Assess this cell for malaria.
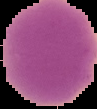

Uninfected.

image_type: cell region segmented out of the field of view; surrounding area masked to black
image_size: 97×109 pixels
preparation: thin blood smear